Report the malaria status of this cell.
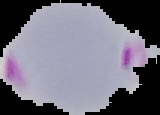

It is parasitized.

preparation: thin blood smear
image_size: 160×115 pixels
image_type: segmented cell region on a black background